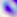
modality: photomicrograph
magnification: 400x
identification: Toxoplasma gondii